State which parasite is depicted.
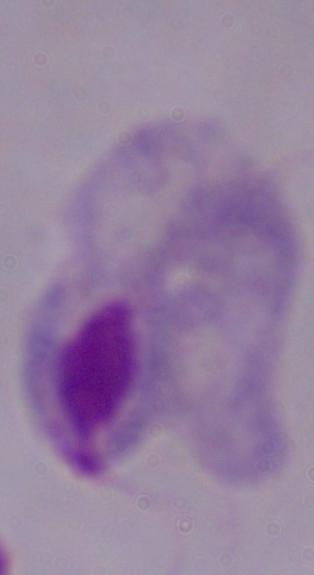
This is a trichomonad.

{
  "magnification": "1000x",
  "modality": "photomicrograph"
}